Assess this cell for malaria.
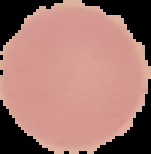

Uninfected.

From a thin blood smear. Image is 151×154 pixels. Segmented cell region on a black background.